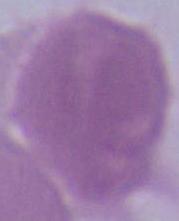

identification = red blood cell
modality = micrograph
magnification = 1000x